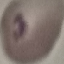

Malaria status: parasitized. Giemsa stain. Cell patch, automatically extracted from a larger field of view and resized to 64 × 64 pixels. Photographed with a smartphone camera at the microscope eyepiece. Thin smear of blood.